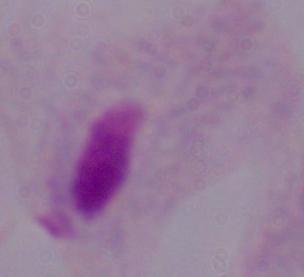
identification: trichomonad
modality: photomicrograph
magnification: 1000x